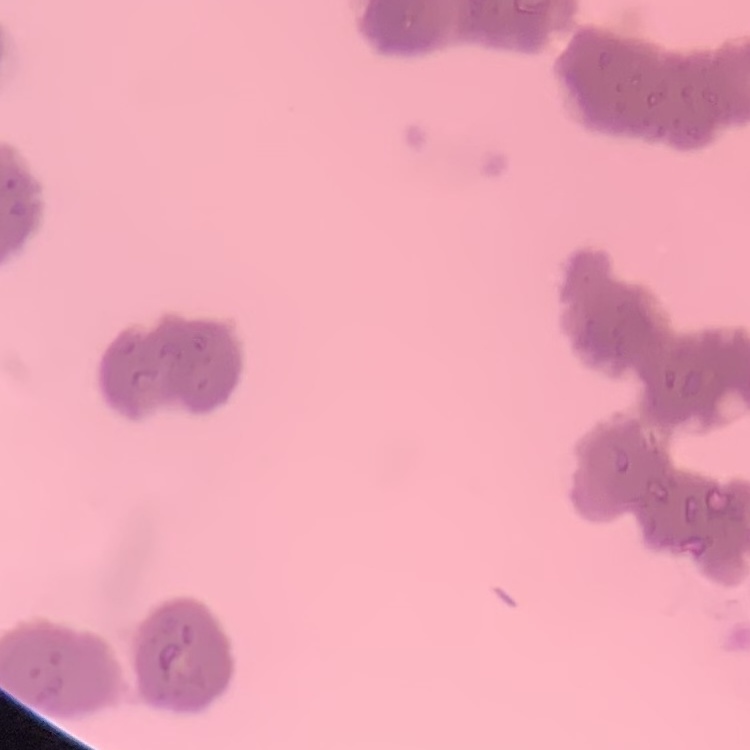

red_blood_cell_morphology: rouleaux formation
image_type: one tile cut from a larger photomicrograph
preparation: thin blood film
stain: Field's or Giemsa